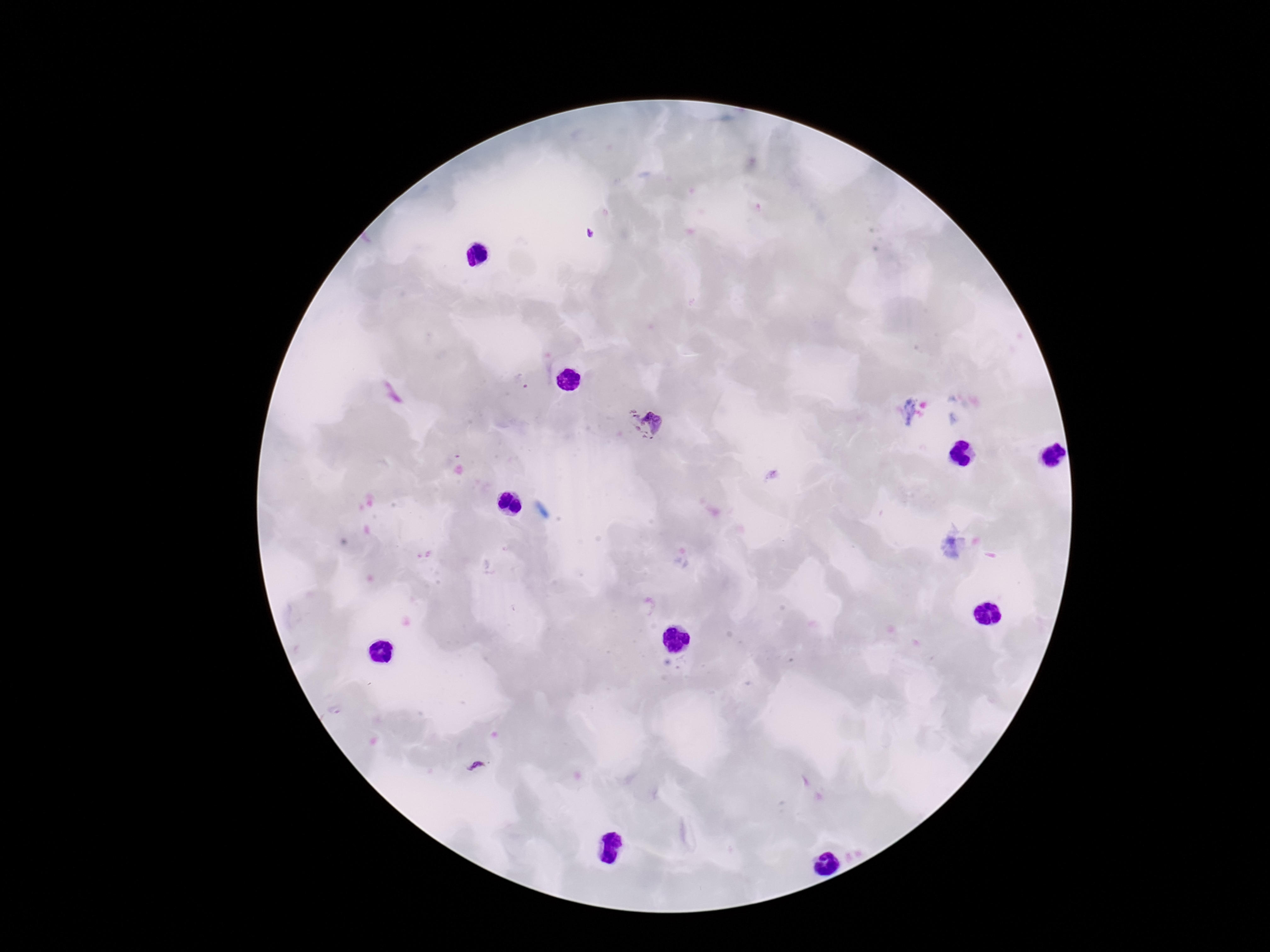

{
  "plasmodium_parasite_locations": "approximate centers as (x, y) in pixels: (589, 235), (520, 383), (646, 422), (477, 767)",
  "preparation": "thick peripheral-blood smear",
  "magnification": "100x",
  "stain": "Giemsa",
  "capture": "smartphone camera through the microscope eyepiece",
  "image_size": "1270×952 pixels",
  "field_of_view": "single",
  "patient_malaria_status": "positive"
}